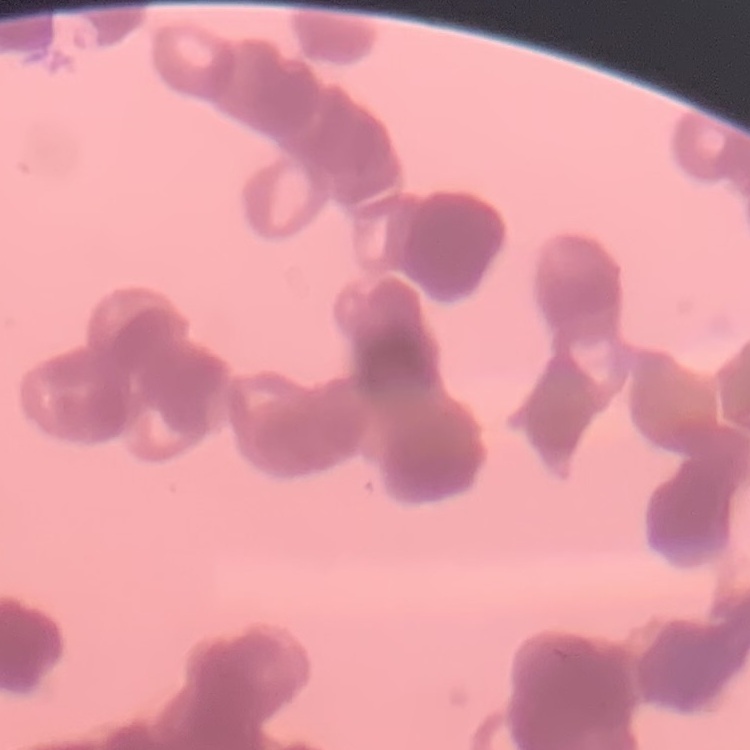
The erythrocytes show rouleaux formation. Stained with either Field's or Giemsa. Thin peripheral smear. Square crop of a larger photomicrograph.